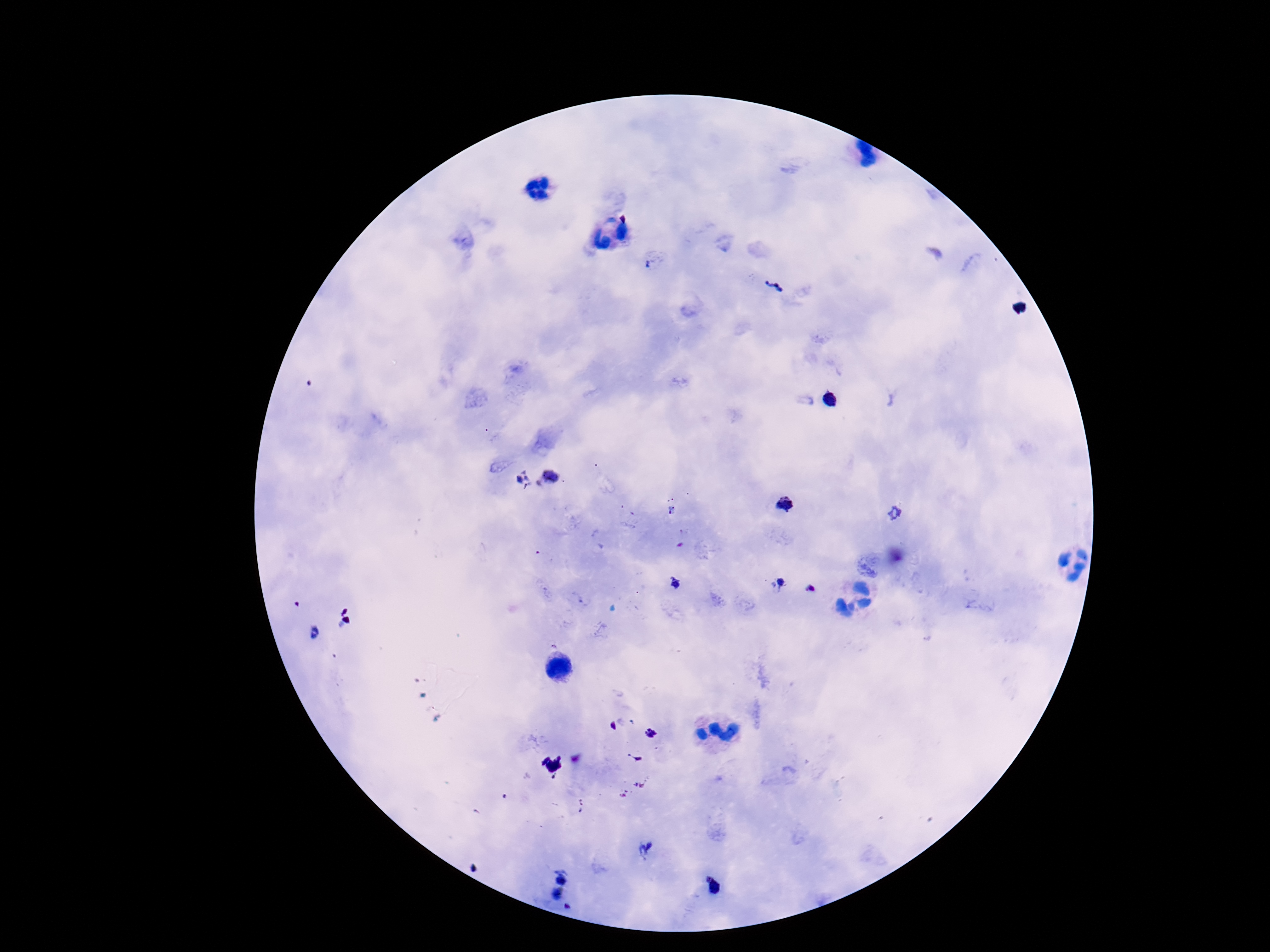

{
  "stain": "Giemsa",
  "image_size": "1270×952 pixels",
  "plasmodium_parasite_locations": "approximate centers as [x, y] in pixels: [651, 266], [774, 286], [551, 478], [523, 480], [785, 505], [895, 515], [778, 583], [674, 584], [810, 589], [314, 633], [648, 850], [562, 874], [715, 887], [558, 895]",
  "capture": "smartphone camera through the microscope eyepiece",
  "field_of_view": "single",
  "patient_malaria_status": "infected",
  "magnification": "100x",
  "preparation": "thick blood smear"
}